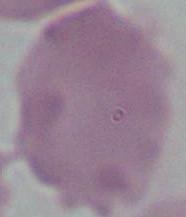

{
  "magnification": "1000x",
  "modality": "micrograph",
  "identification": "erythrocyte"
}